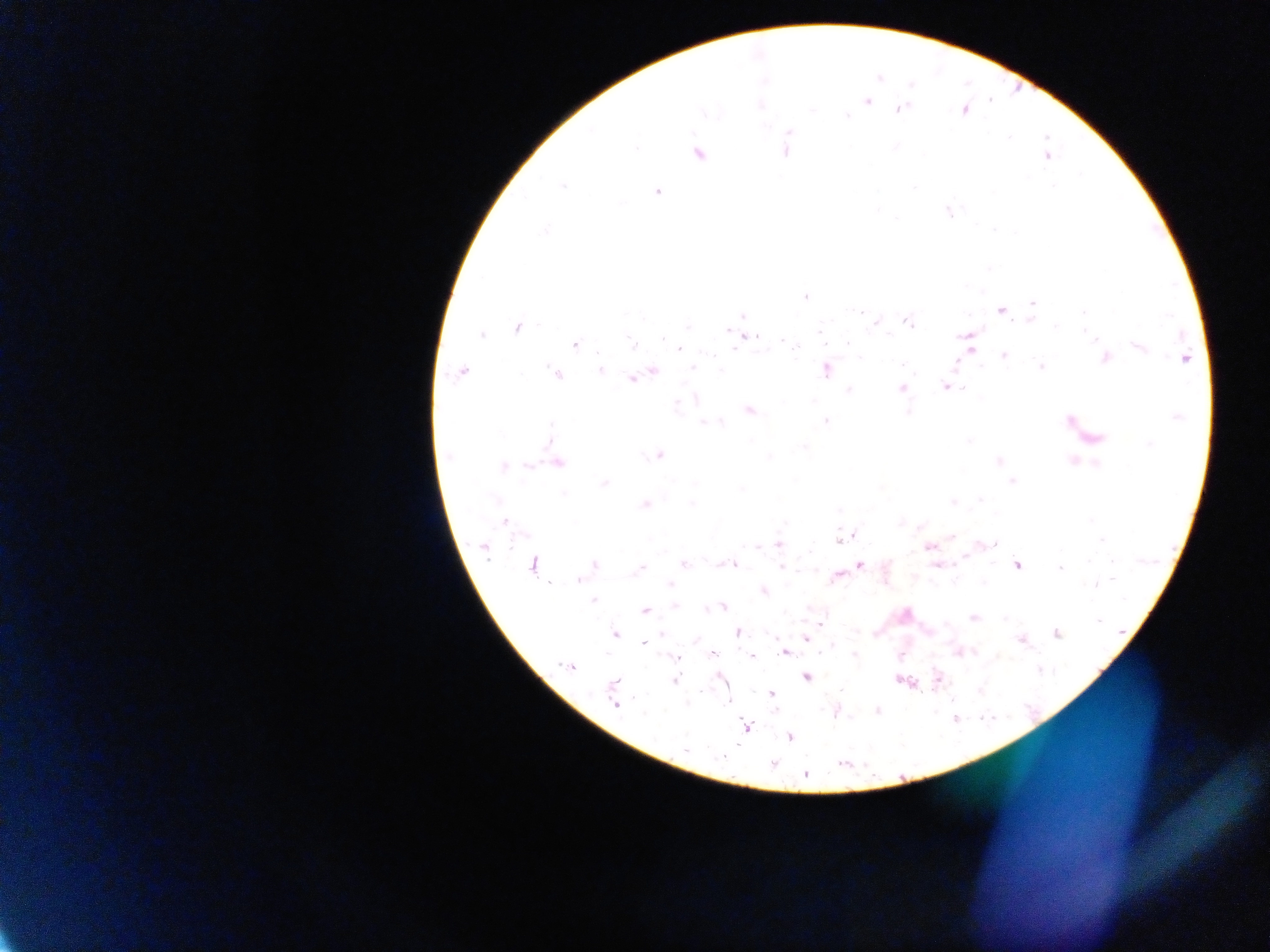
Approximate centers as x y in pixels. Malaria parasite locations: 867 100; 899 109; 785 150; 697 153; 1046 155; 657 191; 948 210; 804 296; 1033 304; 1001 311; 860 312; 1083 312; 742 315; 877 321; 908 321; 517 327; 746 336; 968 339; 575 343; 1140 345; 679 348; 970 349; 1003 355; 1105 358; 1184 358; 1042 367; 692 368; 599 369; 826 369; 652 370; 461 372; 557 374; 639 374; 631 377; 947 385; 900 388; 749 409; 826 420; 1070 421; 1091 438; 659 455; 556 462; 502 466; 1012 481; 604 483; 645 504; 504 521; 851 534; 841 538; 778 543; 929 546; 484 547; 683 564; 724 564; 731 564; 938 564; 1016 564; 533 565; 860 565; 593 566; 1060 566; 781 567; 639 568; 837 575; 670 583; 1096 583; 763 590; 723 606; 646 610; 973 617; 821 622; 737 632; 614 633; 1056 633; 806 638; 1021 639; 645 642; 785 651; 712 654; 751 656; 675 657; 570 666; 720 677; 806 677; 937 677; 674 680; 903 680; 771 693; 614 699; 729 701; 876 710; 836 711; 746 727; 790 736; 684 749; 773 764; 804 774. Photographed through a microscope with a mobile-phone camera. Single field of view. Image is 1270×952 pixels. Sample from Ghana. Thick blood film.